Name the blood parasite species.
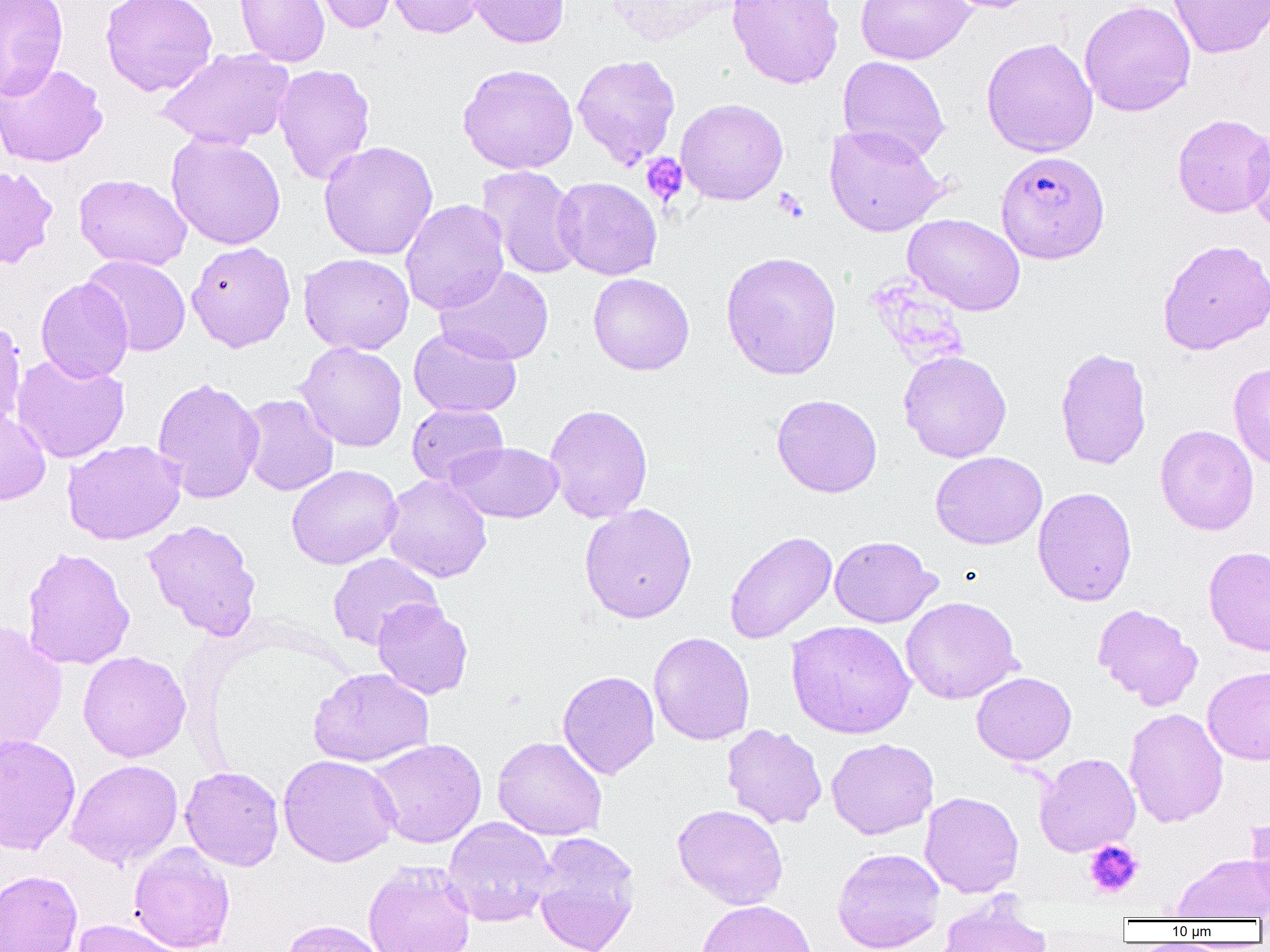
Plasmodium falciparum.

Approximate bounding boxes as (x1, y1, x2, y2) in pixels. Platelet locations: (640, 153, 688, 205), (774, 187, 809, 222), (1084, 840, 1143, 899). Uninfected red blood cell locations: (0, 0, 68, 100), (100, 0, 218, 96), (234, 0, 330, 67), (304, 0, 399, 34), (388, 0, 486, 38), (467, 0, 569, 48), (605, 0, 733, 46), (727, 0, 844, 89), (855, 0, 975, 65), (937, 0, 1044, 13), (1079, 0, 1196, 117), (1168, 0, 1270, 58), (981, 37, 1098, 157), (156, 47, 296, 150), (572, 54, 681, 168), (837, 56, 950, 162), (0, 62, 108, 168), (273, 63, 376, 185), (457, 63, 578, 174), (676, 98, 788, 206), (1172, 113, 1270, 218), (1244, 123, 1270, 238), (824, 124, 949, 237), (166, 133, 286, 250), (318, 140, 438, 261), (0, 165, 59, 269), (476, 165, 585, 280), (74, 173, 192, 270), (552, 177, 662, 281), (400, 199, 509, 315), (903, 213, 1025, 316), (1157, 239, 1270, 355), (186, 241, 296, 352), (721, 250, 842, 380), (298, 253, 414, 355), (81, 254, 191, 357), (435, 265, 554, 366), (588, 273, 694, 375), (35, 277, 134, 383), (0, 318, 26, 430), (409, 326, 522, 418), (295, 341, 408, 452), (1054, 346, 1152, 470), (898, 350, 1012, 463), (11, 353, 130, 464), (1227, 361, 1270, 470), (152, 376, 265, 504), (240, 394, 339, 496), (772, 394, 883, 497), (407, 404, 508, 487), (544, 404, 653, 523), (0, 406, 50, 505), (1155, 425, 1259, 535), (62, 439, 186, 545), (447, 442, 565, 523), (930, 451, 1047, 550), (286, 464, 403, 570), (382, 474, 492, 583), (1033, 486, 1137, 606), (579, 503, 698, 624), (143, 520, 262, 640), (724, 531, 837, 644), (829, 535, 941, 628), (21, 546, 135, 670), (1203, 546, 1270, 656), (327, 553, 442, 650), (900, 596, 1022, 705), (372, 599, 473, 700), (1092, 603, 1203, 710), (785, 620, 917, 740), (0, 621, 68, 756), (648, 632, 755, 746), (78, 650, 191, 762), (1203, 665, 1270, 765), (308, 667, 434, 767), (558, 670, 660, 779), (971, 672, 1076, 765), (1124, 708, 1228, 827), (721, 724, 827, 829), (0, 734, 81, 856), (493, 736, 607, 841), (367, 738, 487, 848), (826, 738, 938, 840), (1035, 753, 1141, 857), (278, 754, 400, 867), (66, 759, 184, 868), (180, 766, 284, 871), (920, 791, 1024, 897), (672, 804, 788, 909), (1245, 813, 1270, 913), (442, 817, 557, 927), (531, 831, 642, 952), (129, 842, 235, 952), (832, 847, 945, 952), (1173, 853, 1270, 921), (363, 860, 476, 952), (0, 870, 82, 952), (935, 894, 1052, 951), (696, 899, 817, 952), (72, 919, 186, 952), (280, 919, 388, 952). Plasmodium falciparum-infected red blood cell locations: (995, 150, 1110, 263). One field of a larger specimen. Thin blood smear. Captured at 1000x magnification. Image is 1270×952 pixels. Optical microscopy.